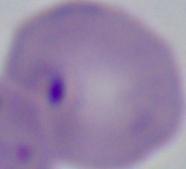
A Babesia parasite is shown. Micrograph. 1000x magnification.